Assess this cell for malaria.
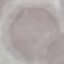

It is uninfected.

{
  "image_type": "automatically extracted cell patch, resized to 64 × 64 pixels",
  "preparation": "thin smear",
  "capture": "smartphone through the microscope eyepiece",
  "stain": "Giemsa"
}